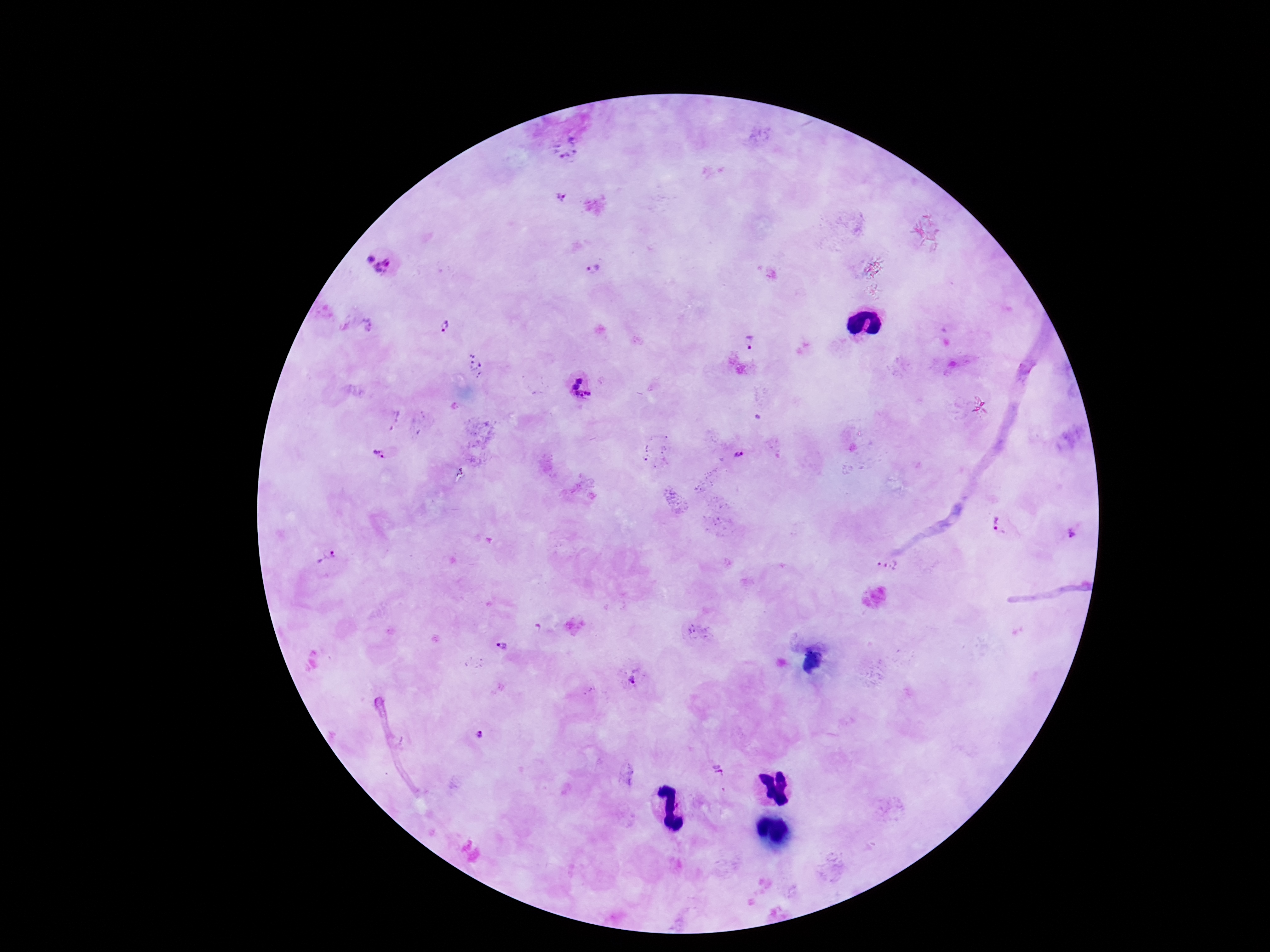
Approximate centers as (x, y) in pixels.
Summary:
  - Plasmodium parasite locations: (567, 150), (560, 198), (380, 263), (590, 270), (446, 326), (748, 342), (582, 387), (381, 455), (738, 455), (1000, 525), (1073, 532), (328, 560), (887, 564), (500, 645), (634, 677), (477, 738), (719, 772)
  - Preparation: thick peripheral-blood smear
  - Field of view: one from this slide
  - Stain: Giemsa
  - Image size: 1270×952 pixels
  - Patient malaria status: infected
  - Capture: smartphone camera through the microscope eyepiece
  - Magnification: 100x